Assess this cell for malaria.
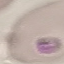

It is parasitized.

image type = automatically extracted cell patch, resized to 64 × 64 pixels
capture = smartphone through the microscope eyepiece
preparation = thin blood smear
stain = Giemsa